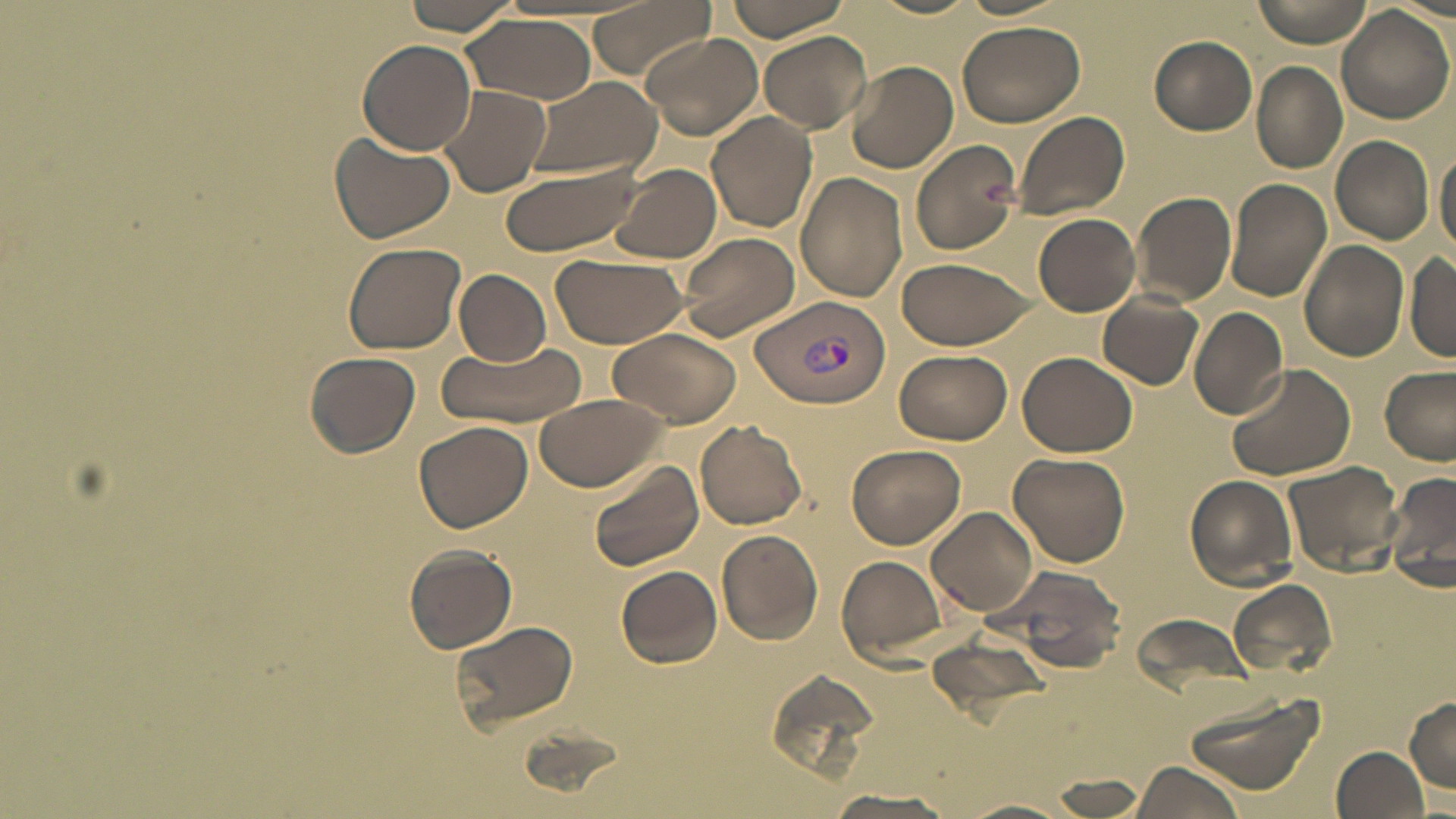
{
  "slide_level_diagnosis": "Plasmodium vivax",
  "platelet_locations": "approximate bounding boxes as named x1/y1/x2/y2 corners in pixels: (x1=980, y1=179, x2=1015, y2=211)",
  "plasmodium_vivax_infected_red_blood_cell_locations": "approximate bounding boxes as named x1/y1/x2/y2 corners in pixels: (x1=755, y1=295, x2=890, y2=406)",
  "modality": "optical microscopy",
  "field_of_view": "one of a larger specimen",
  "preparation": "thin blood film",
  "magnification": "1000x",
  "stain": "May-Grünwald-Giemsa",
  "uninfected_red_blood_cell_locations": "approximate bounding boxes as named x1/y1/x2/y2 corners in pixels: (x1=400, y1=0, x2=522, y2=35), (x1=585, y1=0, x2=712, y2=81), (x1=722, y1=0, x2=854, y2=41), (x1=867, y1=0, x2=983, y2=19), (x1=1251, y1=0, x2=1375, y2=46), (x1=1335, y1=6, x2=1455, y2=126), (x1=464, y1=15, x2=596, y2=104), (x1=955, y1=19, x2=1086, y2=127), (x1=758, y1=31, x2=872, y2=133), (x1=639, y1=32, x2=764, y2=140), (x1=1149, y1=37, x2=1257, y2=134), (x1=358, y1=38, x2=476, y2=154), (x1=845, y1=61, x2=959, y2=174), (x1=1250, y1=61, x2=1347, y2=173), (x1=523, y1=76, x2=662, y2=181), (x1=438, y1=86, x2=551, y2=197), (x1=1013, y1=109, x2=1127, y2=222), (x1=706, y1=110, x2=818, y2=233), (x1=328, y1=130, x2=456, y2=242), (x1=1329, y1=135, x2=1435, y2=245), (x1=912, y1=139, x2=1024, y2=257), (x1=1434, y1=144, x2=1456, y2=259), (x1=498, y1=160, x2=647, y2=257), (x1=609, y1=164, x2=723, y2=263), (x1=795, y1=171, x2=907, y2=301), (x1=1224, y1=177, x2=1332, y2=301), (x1=1131, y1=191, x2=1236, y2=305), (x1=1033, y1=212, x2=1141, y2=316), (x1=674, y1=232, x2=801, y2=343), (x1=1299, y1=240, x2=1408, y2=363), (x1=341, y1=243, x2=464, y2=355), (x1=550, y1=253, x2=686, y2=347), (x1=1406, y1=254, x2=1456, y2=361), (x1=897, y1=256, x2=1034, y2=350), (x1=454, y1=267, x2=551, y2=366), (x1=1099, y1=292, x2=1205, y2=390), (x1=1188, y1=306, x2=1289, y2=420), (x1=610, y1=328, x2=739, y2=428), (x1=436, y1=340, x2=587, y2=429), (x1=894, y1=349, x2=1012, y2=445), (x1=304, y1=350, x2=419, y2=456), (x1=1017, y1=350, x2=1137, y2=458), (x1=1229, y1=363, x2=1356, y2=480), (x1=1378, y1=365, x2=1455, y2=464), (x1=534, y1=394, x2=668, y2=492), (x1=695, y1=419, x2=808, y2=530), (x1=413, y1=421, x2=533, y2=534), (x1=846, y1=444, x2=966, y2=548), (x1=1007, y1=451, x2=1131, y2=566), (x1=1284, y1=460, x2=1405, y2=577), (x1=586, y1=461, x2=703, y2=574), (x1=1385, y1=468, x2=1456, y2=591), (x1=1185, y1=475, x2=1299, y2=587), (x1=925, y1=506, x2=1039, y2=617), (x1=716, y1=529, x2=824, y2=646), (x1=404, y1=545, x2=518, y2=653), (x1=836, y1=553, x2=951, y2=665), (x1=993, y1=563, x2=1129, y2=674), (x1=616, y1=565, x2=722, y2=668), (x1=1228, y1=580, x2=1337, y2=681), (x1=1128, y1=612, x2=1250, y2=695), (x1=446, y1=618, x2=578, y2=736), (x1=925, y1=631, x2=1057, y2=725), (x1=763, y1=664, x2=883, y2=784), (x1=1180, y1=688, x2=1326, y2=800), (x1=1405, y1=696, x2=1456, y2=792), (x1=1331, y1=745, x2=1429, y2=819), (x1=1128, y1=760, x2=1246, y2=819), (x1=1047, y1=776, x2=1154, y2=816), (x1=823, y1=786, x2=959, y2=818), (x1=963, y1=798, x2=1083, y2=819)",
  "image_size": "1456×819 pixels"
}